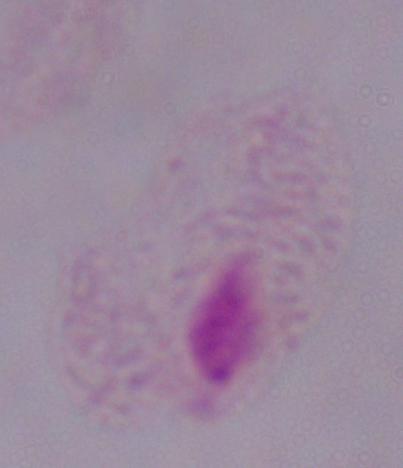

Summary:
  - Magnification: 1000x
  - Modality: micrograph
  - Identification: trichomonad